Describe the morphology of the red blood cells.
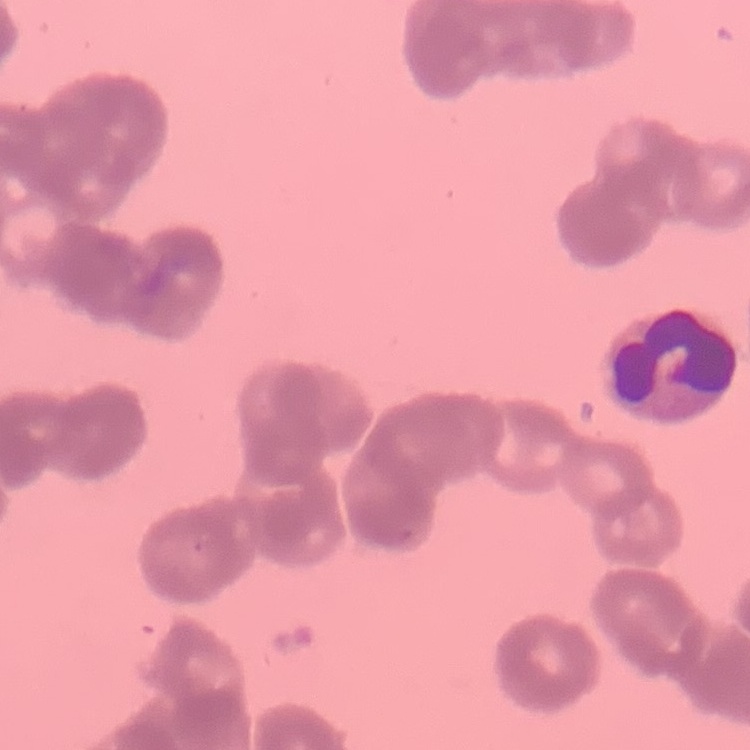

Rouleaux formation.

Thin blood smear. One tile cut from a larger photomicrograph. Field's or Giemsa stain.